Look for Plasmodium parasites.
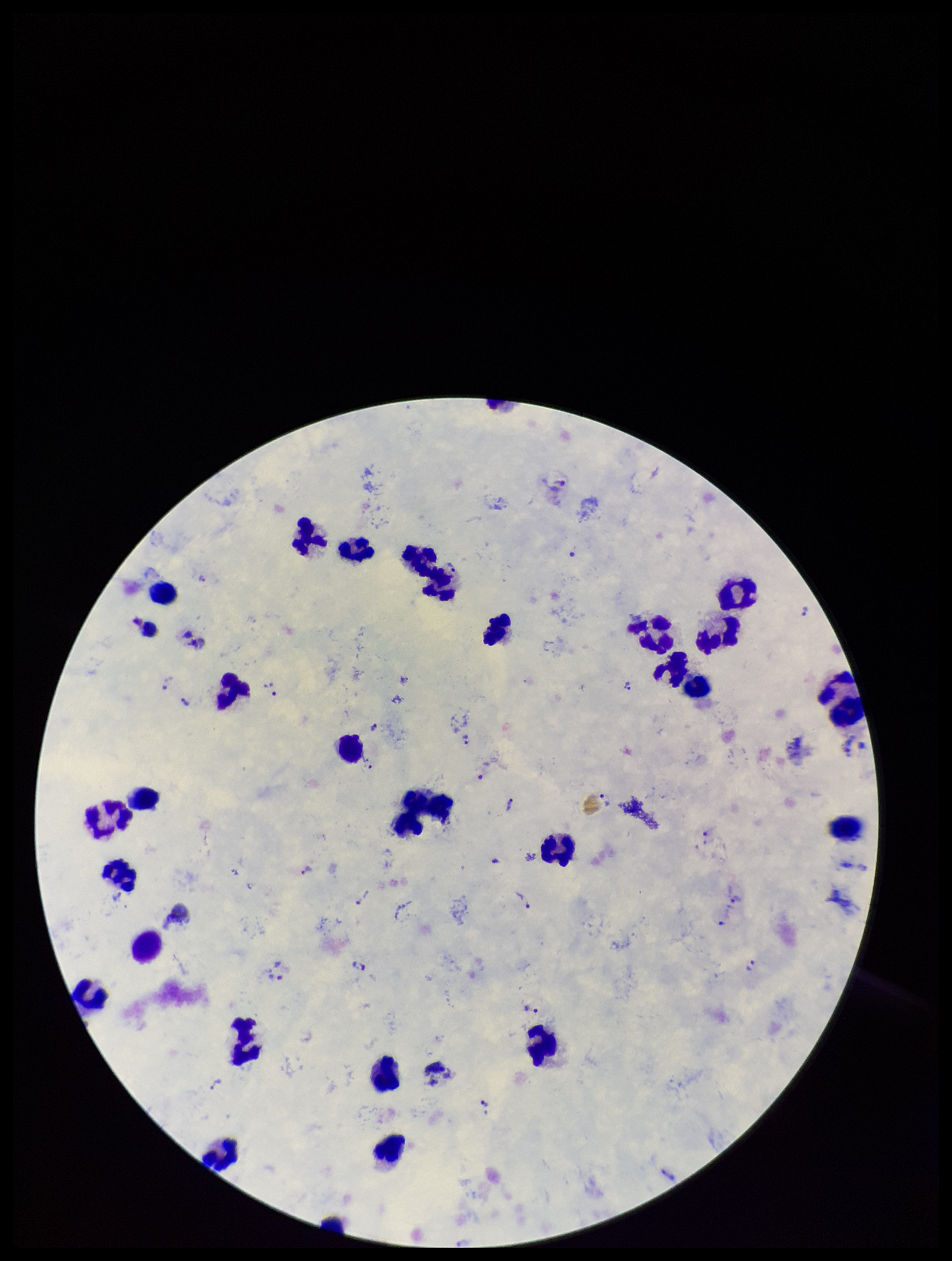

Detected.

Summary:
  - Field of view: single
  - Leukocyte count: 26
  - Image size: 952×1261 pixels
  - Patient malaria status: infected
  - Parasite count: 25
  - Species reported for this patient: Plasmodium vivax
  - Capture: smartphone photograph through the microscope eyepiece
  - Preparation: thick
  - Stain: Giemsa